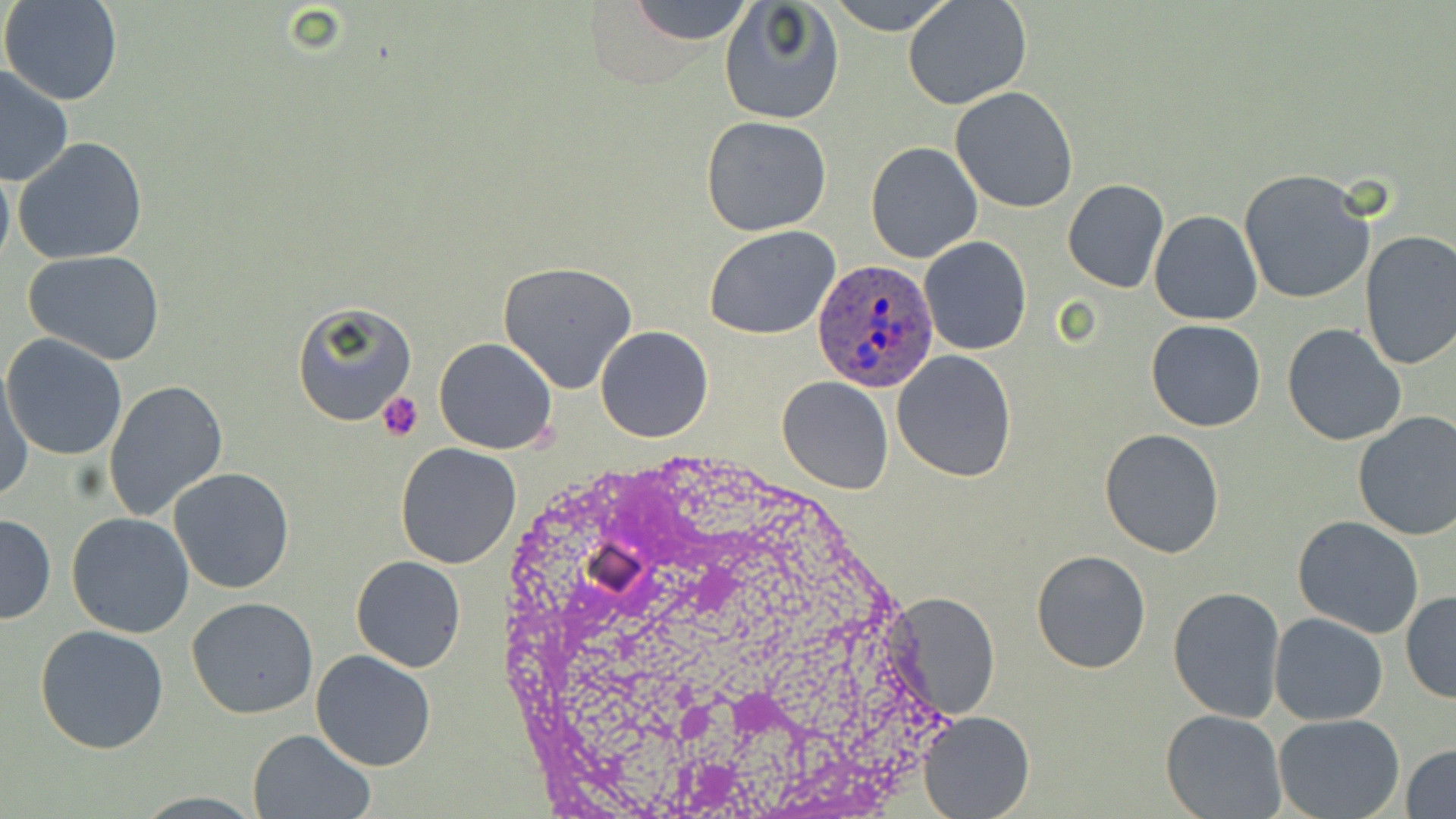
Approximate bounding boxes as (x1, y1, x2, y2) in pixels. Plasmodium ovale-infected red blood cell locations: (809, 257, 940, 391). Platelet locations: (375, 391, 424, 441). Uninfected red blood cell locations: (2, 0, 124, 107), (626, 0, 756, 44), (827, 0, 959, 36), (904, 0, 1033, 110), (718, 2, 845, 125), (0, 66, 76, 188), (949, 86, 1078, 213), (700, 115, 832, 237), (14, 137, 148, 264), (865, 141, 983, 263), (0, 164, 14, 273), (1238, 168, 1376, 305), (1062, 178, 1170, 292), (1150, 211, 1262, 326), (704, 226, 843, 342), (1357, 229, 1456, 371), (919, 236, 1032, 356), (25, 251, 166, 365), (498, 261, 641, 394), (290, 299, 416, 428), (1147, 320, 1265, 432), (1281, 324, 1406, 446), (594, 326, 713, 443), (2, 334, 129, 462), (433, 337, 558, 455), (892, 349, 1018, 482), (1, 368, 33, 501), (776, 376, 892, 495), (105, 380, 230, 524), (1352, 412, 1456, 541), (1098, 428, 1224, 558), (395, 442, 522, 570), (169, 466, 294, 595), (0, 513, 55, 624), (66, 513, 195, 639), (1293, 516, 1424, 640), (1031, 549, 1151, 674), (350, 556, 466, 672), (1167, 585, 1286, 722), (886, 592, 1001, 722), (1401, 592, 1456, 704), (186, 598, 318, 720), (1269, 612, 1390, 726), (35, 626, 170, 754), (310, 649, 437, 771), (918, 709, 1035, 819), (1161, 709, 1288, 819), (1273, 714, 1404, 819), (248, 729, 374, 818), (1403, 742, 1456, 818). Slide-level diagnosis: Plasmodium ovale. Thin blood smear. One field of a larger specimen. May-Grünwald-Giemsa-stained preparation. Optical microscopy. 1000x magnification. Image is 1456×819 pixels.